Assess for Plasmodium parasites.
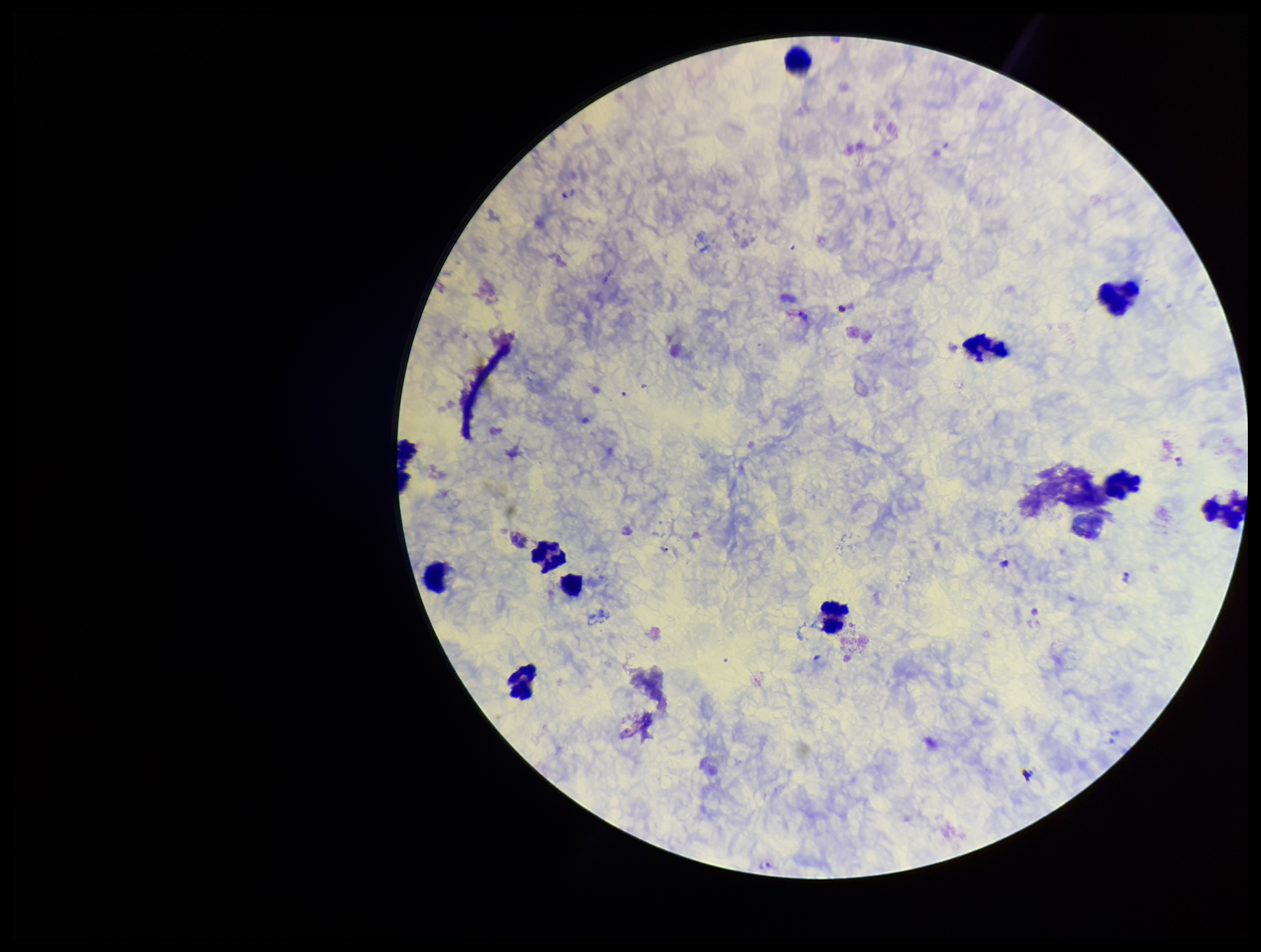

Identified.

Patient malaria status: infected. Parasite count: 6. Species reported for this patient: Plasmodium vivax. Image is 1261×952 pixels. Photographed through the microscope eyepiece with a smartphone camera. Preparation: thick. Leukocyte count: 12. Giemsa stain. Single field of view.